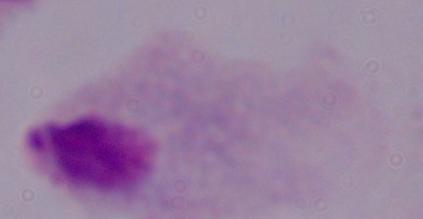
Summary:
  - Identification: trichomonad
  - Modality: micrograph
  - Magnification: 1000x